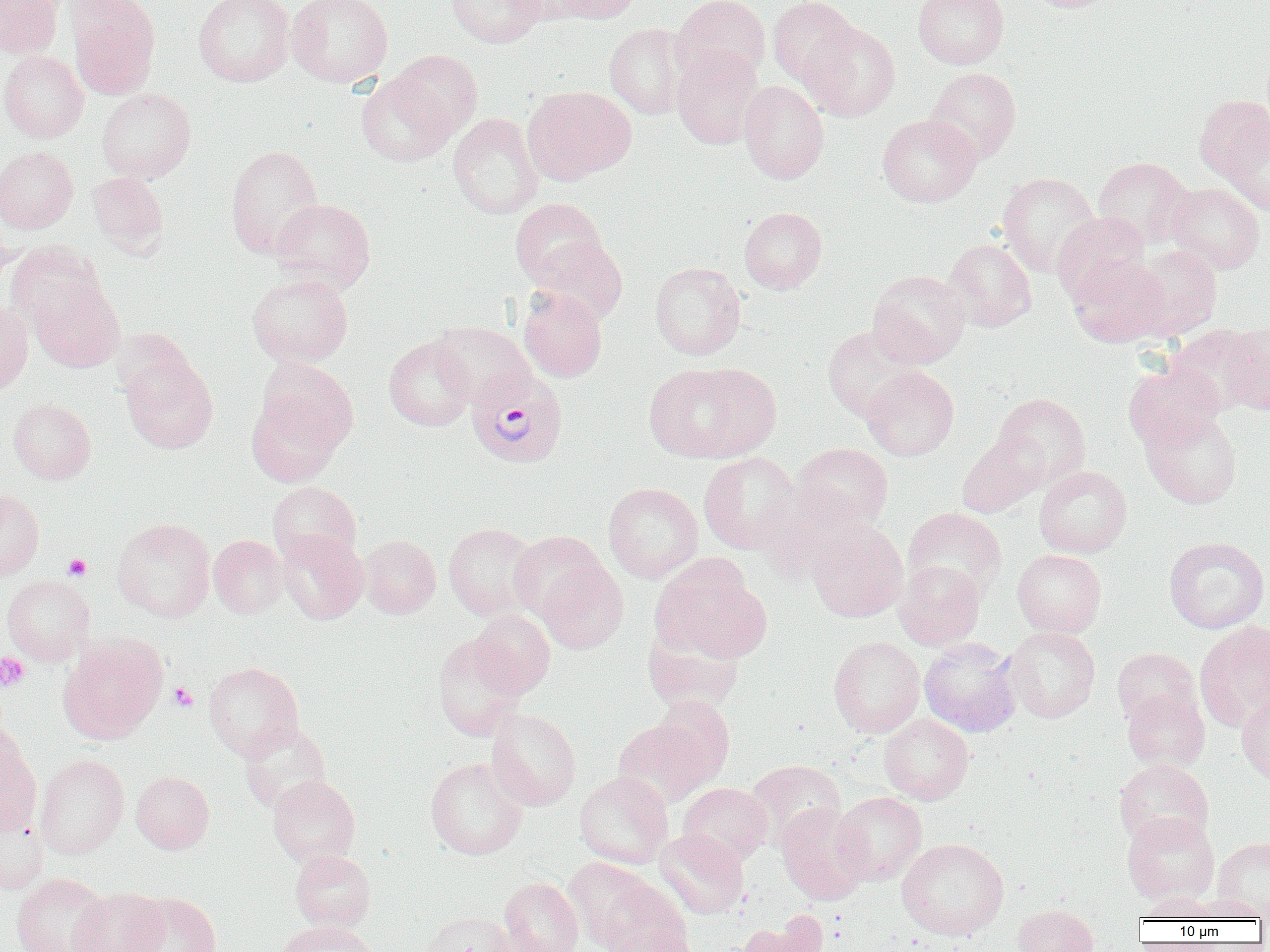

Summary:
  - Coordinate format: approximate bounding boxes as [x1, y1, x2, y2] in pixels
  - Platelet locations: [64, 554, 91, 580], [0, 653, 30, 692], [168, 682, 198, 713]
  - Plasmodium vivax-infected red blood cell locations: [466, 365, 569, 468]
  - Uninfected red blood cell locations: [0, 0, 63, 58], [66, 0, 160, 100], [193, 0, 295, 87], [287, 0, 393, 87], [446, 0, 546, 48], [507, 0, 588, 24], [555, 0, 641, 24], [672, 0, 770, 84], [768, 0, 859, 87], [913, 0, 1009, 69], [1025, 0, 1119, 13], [800, 21, 901, 121], [605, 23, 691, 119], [671, 46, 764, 150], [0, 50, 88, 143], [387, 50, 482, 140], [925, 67, 1021, 163], [356, 72, 456, 166], [739, 80, 829, 184], [524, 85, 636, 183], [97, 88, 196, 183], [1195, 94, 1270, 185], [448, 113, 543, 219], [877, 113, 981, 207], [1223, 120, 1270, 215], [225, 144, 325, 258], [1, 146, 78, 234], [1093, 156, 1195, 248], [87, 172, 168, 257], [997, 172, 1101, 277], [1165, 182, 1265, 274], [271, 198, 375, 294], [510, 198, 607, 288], [739, 206, 827, 293], [1052, 212, 1150, 306], [0, 229, 17, 291], [532, 237, 627, 325], [942, 238, 1037, 332], [6, 242, 107, 331], [1130, 245, 1221, 341], [1068, 256, 1169, 348], [649, 262, 746, 360], [868, 269, 971, 368], [247, 273, 353, 368], [30, 279, 125, 372], [518, 287, 607, 382], [0, 300, 33, 396], [430, 321, 533, 407], [1219, 322, 1270, 415], [1167, 324, 1264, 416], [822, 326, 924, 422], [384, 336, 476, 431], [122, 354, 218, 454], [257, 359, 357, 453], [1123, 360, 1224, 452], [644, 361, 778, 463], [862, 365, 959, 461], [246, 392, 344, 487], [993, 392, 1091, 486], [8, 398, 96, 484], [1142, 410, 1242, 508], [956, 432, 1048, 518], [792, 442, 893, 531], [699, 452, 800, 554], [1034, 466, 1132, 558], [268, 481, 361, 565], [603, 482, 703, 583], [763, 488, 874, 582], [0, 489, 44, 579], [903, 507, 1007, 601], [112, 518, 215, 622], [806, 522, 908, 622], [443, 523, 540, 619], [276, 530, 367, 625], [508, 531, 607, 621], [208, 535, 287, 618], [359, 535, 440, 618], [1164, 537, 1269, 633], [1012, 549, 1107, 638], [650, 554, 767, 662], [539, 560, 627, 654], [893, 560, 986, 650], [1, 575, 94, 665], [469, 609, 555, 698], [1194, 621, 1270, 733], [642, 623, 745, 713], [1004, 626, 1100, 723], [59, 633, 167, 743], [433, 634, 526, 740], [828, 636, 925, 738], [919, 638, 1022, 737], [1112, 648, 1201, 727], [203, 662, 303, 760], [1122, 688, 1210, 772], [651, 695, 735, 785], [1236, 695, 1270, 786], [486, 708, 581, 811], [879, 714, 973, 805], [613, 719, 714, 808], [238, 721, 332, 814], [0, 729, 40, 833], [35, 754, 129, 859], [425, 756, 528, 860], [1114, 759, 1213, 847], [745, 760, 846, 850], [131, 771, 214, 853], [574, 771, 674, 869], [267, 774, 360, 866], [679, 782, 772, 866], [832, 792, 926, 886], [776, 802, 870, 905], [0, 805, 49, 894], [1122, 812, 1220, 904], [655, 829, 748, 919], [1213, 836, 1270, 917], [897, 837, 1008, 940], [290, 849, 375, 932], [564, 857, 658, 950], [11, 872, 111, 952], [499, 877, 583, 952], [595, 877, 692, 952], [69, 888, 167, 952], [124, 892, 222, 952], [1137, 892, 1219, 922], [1187, 895, 1267, 922], [1012, 904, 1098, 952], [418, 911, 515, 952], [734, 917, 829, 952], [275, 921, 377, 952], [608, 929, 701, 952]
  - Slide-level diagnosis: Plasmodium vivax
  - Preparation: thin blood smear
  - Modality: optical microscopy
  - Image size: 1270×952 pixels
  - Magnification: 1000x
  - Field of view: one of a larger specimen